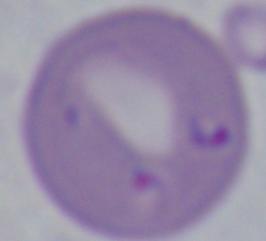

Summary:
  - Identification: Babesia
  - Modality: photomicrograph
  - Magnification: 1000x